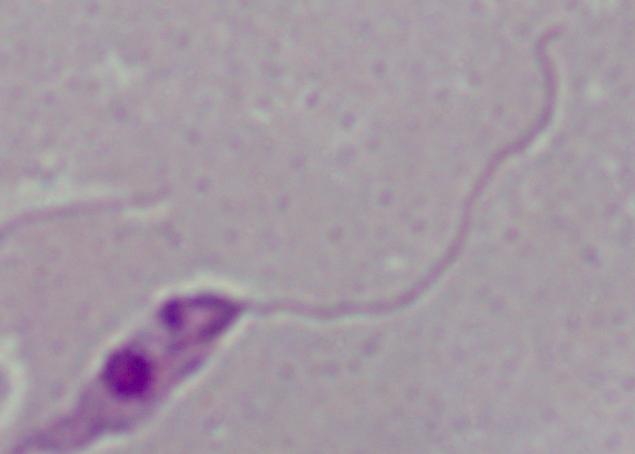

modality = micrograph
identification = Leishmania
magnification = 1000x